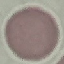
Summary:
  - Result: no malaria parasites detected
  - Image type: cell patch, automatically extracted from a larger field of view and resized to 64 × 64 pixels
  - Preparation: thin blood smear
  - Capture: smartphone camera at the microscope eyepiece
  - Stain: Giemsa